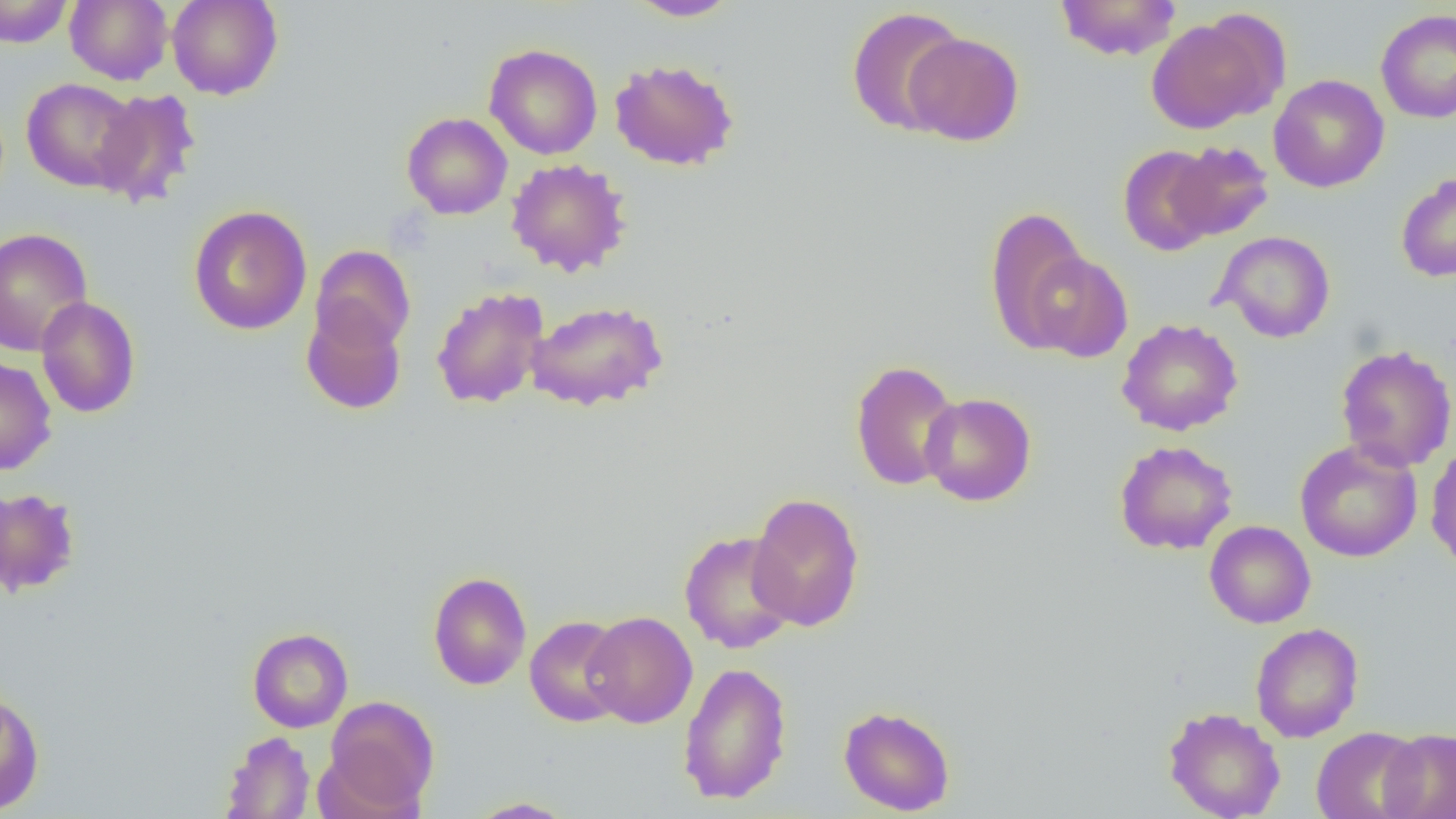

Summary:
  - Coordinate format: approximate bounding boxes as [x1, y1, x2, y2] in pixels
  - Uninfected red blood cell locations: [0, 0, 74, 48], [64, 0, 173, 85], [167, 0, 283, 100], [1055, 0, 1181, 61], [625, 1, 741, 21], [845, 6, 967, 136], [1376, 9, 1456, 124], [1146, 16, 1277, 134], [904, 32, 1025, 146], [484, 43, 603, 160], [609, 58, 740, 171], [1269, 74, 1389, 193], [21, 78, 143, 193], [91, 89, 202, 209], [402, 112, 513, 219], [1166, 140, 1275, 241], [1117, 145, 1220, 256], [505, 158, 632, 277], [1396, 171, 1456, 282], [188, 205, 313, 335], [984, 207, 1091, 349], [0, 227, 93, 357], [1212, 231, 1336, 343], [310, 244, 416, 354], [1018, 249, 1133, 363], [431, 286, 549, 409], [36, 296, 141, 419], [526, 299, 669, 411], [301, 304, 407, 415], [1116, 318, 1243, 436], [1335, 343, 1456, 472], [0, 355, 57, 476], [849, 360, 962, 491], [920, 392, 1037, 506], [1295, 439, 1423, 562], [1113, 440, 1238, 555], [1425, 444, 1456, 573], [0, 488, 81, 597], [748, 492, 865, 632], [1204, 520, 1315, 629], [679, 530, 797, 654], [428, 571, 532, 690], [583, 611, 697, 728], [525, 614, 630, 727], [1250, 623, 1364, 742], [247, 627, 354, 732], [677, 662, 793, 805], [0, 688, 45, 815], [323, 696, 439, 813], [838, 705, 955, 816], [1163, 706, 1286, 819], [1311, 726, 1426, 819], [1378, 728, 1456, 819], [220, 730, 315, 818], [465, 798, 576, 818]
  - Slide-level diagnosis: negative for blood parasites
  - Modality: light microscopy
  - Image size: 1456×819 pixels
  - Preparation: thin blood smear
  - Magnification: 1000x
  - Field of view: one of a larger specimen